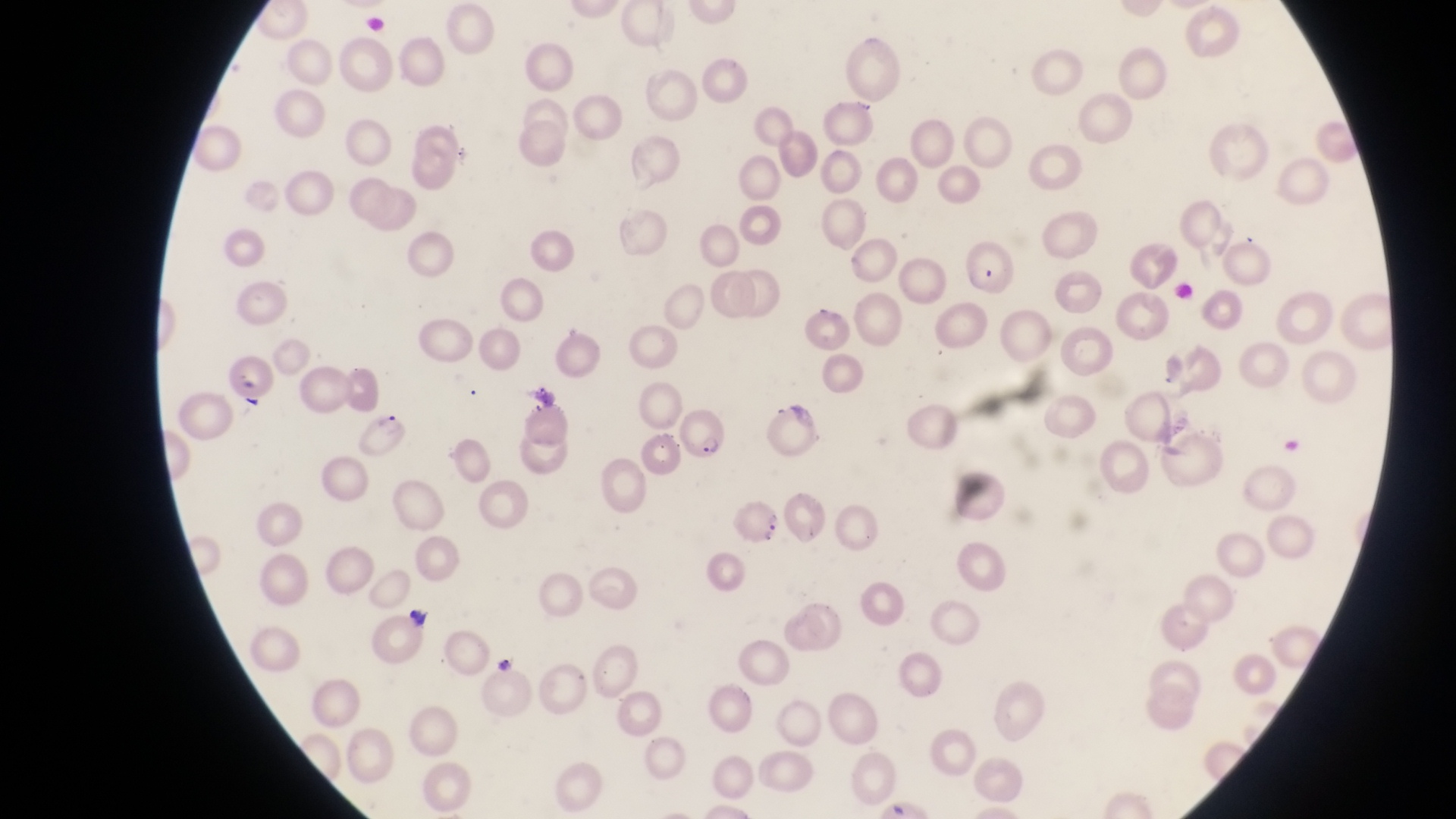
Approximate bounding boxes as (left, top, right, bottom) in pixels. Artifact (platelet-like body, stain precipitate, or debris) locations: (406, 603, 432, 630). Parasitised red blood cell locations: (961, 245, 1019, 294), (222, 357, 274, 402), (761, 402, 819, 452), (671, 404, 726, 462), (357, 412, 407, 459), (729, 500, 793, 556). Photographed through the eyepiece of an Olympus CX-23 microscope with a smartphone camera. Sample from Uganda. At a magnification of 1000x. Image is 1456×819 pixels. Thin blood film. One field of view.